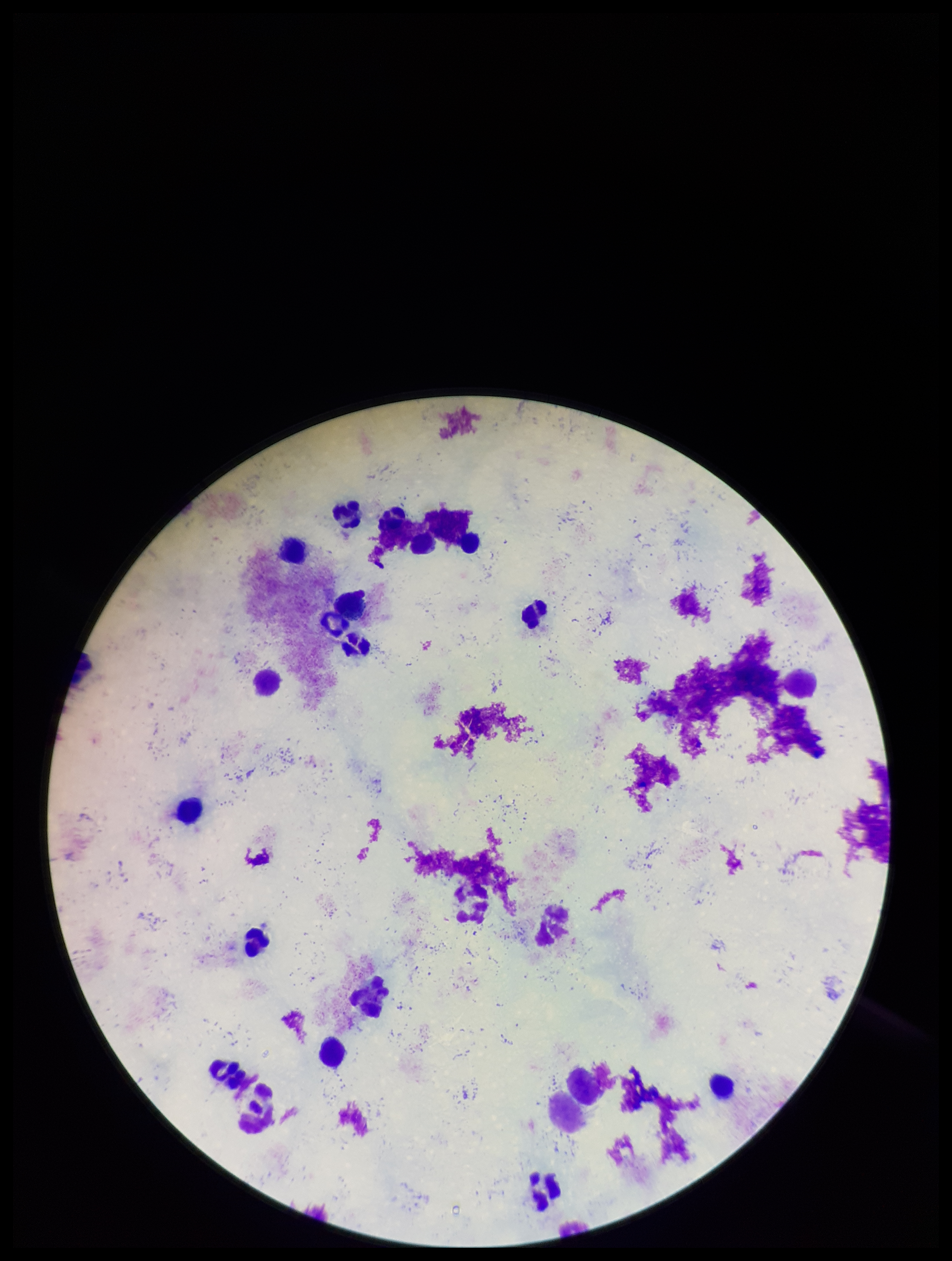
Leukocyte count: 18. Image is 952×1261 pixels. Single field of view. Preparation: thick blood smear. Smartphone photograph taken through the eyepiece of a microscope. Stained with Giemsa. Parasite count: 0. Patient malaria status: negative. Plasmodium parasites: none detected.